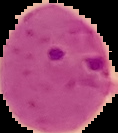
Summary:
  - Malaria status: parasitized
  - Preparation: thin blood smear
  - Image type: segmented cell region on a black background
  - Image size: 118×133 pixels